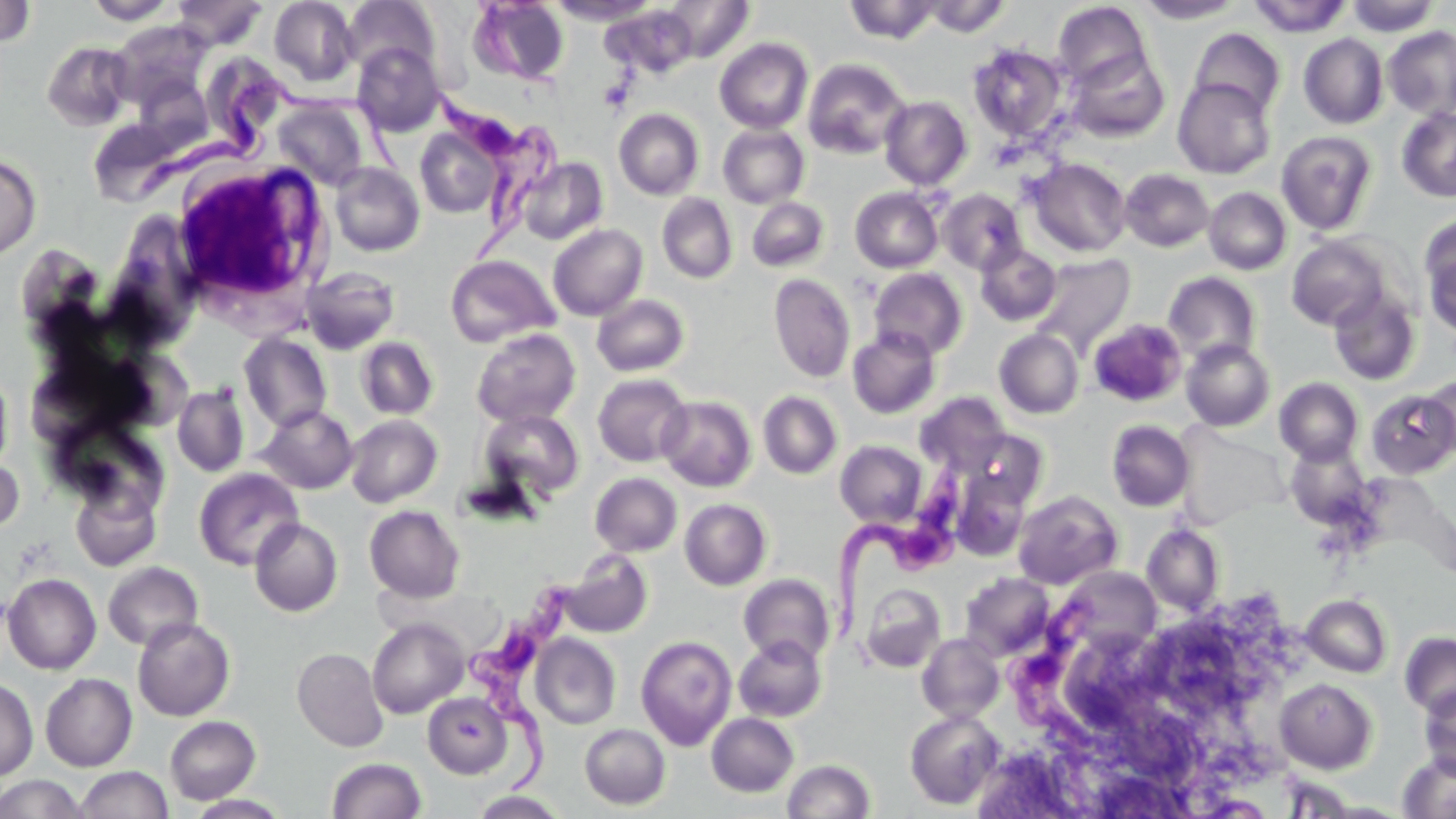

Summary:
  - Coordinate format: approximate bounding boxes as (x1,y1)-(x2,y2) corner pairs in pixels
  - Uninfected red blood cell locations: (85,0)-(180,25), (171,0)-(269,49), (269,0)-(359,87), (341,0)-(440,79), (469,0)-(569,85), (547,0)-(660,25), (661,0)-(754,61), (843,0)-(944,44), (923,0)-(1011,37), (1248,0)-(1352,38), (1346,0)-(1439,36), (0,1)-(35,47), (1135,1)-(1245,23), (1053,2)-(1153,89), (598,6)-(697,78), (110,20)-(212,109), (1383,26)-(1456,118), (1188,28)-(1286,120), (1298,33)-(1389,129), (715,38)-(814,133), (42,41)-(135,131), (352,42)-(445,135), (967,44)-(1069,142), (1065,50)-(1170,143), (205,54)-(291,131), (802,58)-(910,159), (1172,77)-(1276,180), (880,96)-(972,190), (273,98)-(369,191), (1396,107)-(1456,202), (614,108)-(704,200), (88,116)-(180,205), (718,124)-(810,208), (415,127)-(502,218), (1276,131)-(1378,236), (0,154)-(41,259), (517,157)-(608,245), (1027,158)-(1132,257), (330,162)-(424,257), (1119,169)-(1214,252), (851,187)-(944,273), (1204,187)-(1291,275), (937,189)-(1027,275), (657,193)-(738,283), (747,197)-(829,272), (1420,215)-(1456,336), (548,224)-(648,321), (1286,234)-(1393,330), (975,243)-(1061,326), (14,246)-(105,334), (1030,253)-(1136,354), (445,255)-(560,348), (301,266)-(400,354), (869,267)-(967,359), (1163,272)-(1262,364), (769,273)-(855,383), (1328,288)-(1422,386), (592,294)-(689,377), (1089,318)-(1188,407), (848,327)-(941,419), (472,328)-(581,427), (994,329)-(1084,419), (238,333)-(332,432), (356,336)-(439,420), (1181,339)-(1275,431), (0,369)-(14,473), (593,373)-(692,466), (1421,374)-(1456,460), (1275,377)-(1364,466), (172,385)-(250,477), (1365,390)-(1454,480), (758,391)-(842,479), (916,392)-(1011,475), (657,395)-(757,491), (256,405)-(357,494), (479,408)-(585,501), (344,414)-(442,507), (51,418)-(171,519), (1106,420)-(1195,512), (968,430)-(1048,509), (836,440)-(927,528), (1284,442)-(1372,530), (0,452)-(24,537), (193,467)-(303,570), (951,468)-(1032,562), (590,473)-(682,556), (71,481)-(161,570), (1012,491)-(1122,589), (680,498)-(771,590), (364,505)-(465,603), (249,518)-(343,616), (1142,524)-(1225,615), (562,550)-(652,637), (103,561)-(203,651), (1059,567)-(1162,657), (960,572)-(1055,660), (2,573)-(101,674), (739,574)-(835,665), (859,583)-(946,672), (1301,594)-(1392,677), (132,617)-(235,721), (367,618)-(468,718), (1400,631)-(1456,718), (917,633)-(1005,723), (530,634)-(621,729), (635,635)-(737,750), (733,635)-(826,722), (292,647)-(389,752), (40,673)-(137,771), (0,678)-(38,781), (1275,679)-(1377,773), (1419,684)-(1456,777), (422,691)-(513,778), (904,709)-(1004,810), (706,713)-(798,797), (164,716)-(261,804), (580,724)-(670,809), (1397,751)-(1456,817), (326,757)-(426,818), (782,759)-(875,818), (76,766)-(172,819), (0,774)-(87,818), (470,791)-(569,818)
  - Trypanosoma brucei locations: (137,69)-(403,198), (426,85)-(567,281), (830,456)-(975,650), (468,577)-(580,805), (1011,588)-(1109,750)
  - White blood cell locations: (168,158)-(332,310)
  - Slide-level diagnosis: Trypanosoma brucei
  - Preparation: thin blood smear
  - Image size: 1456×819 pixels
  - Modality: optical microscopy
  - Field of view: single
  - Magnification: 1000x
  - Stain: May-Grünwald-Giemsa